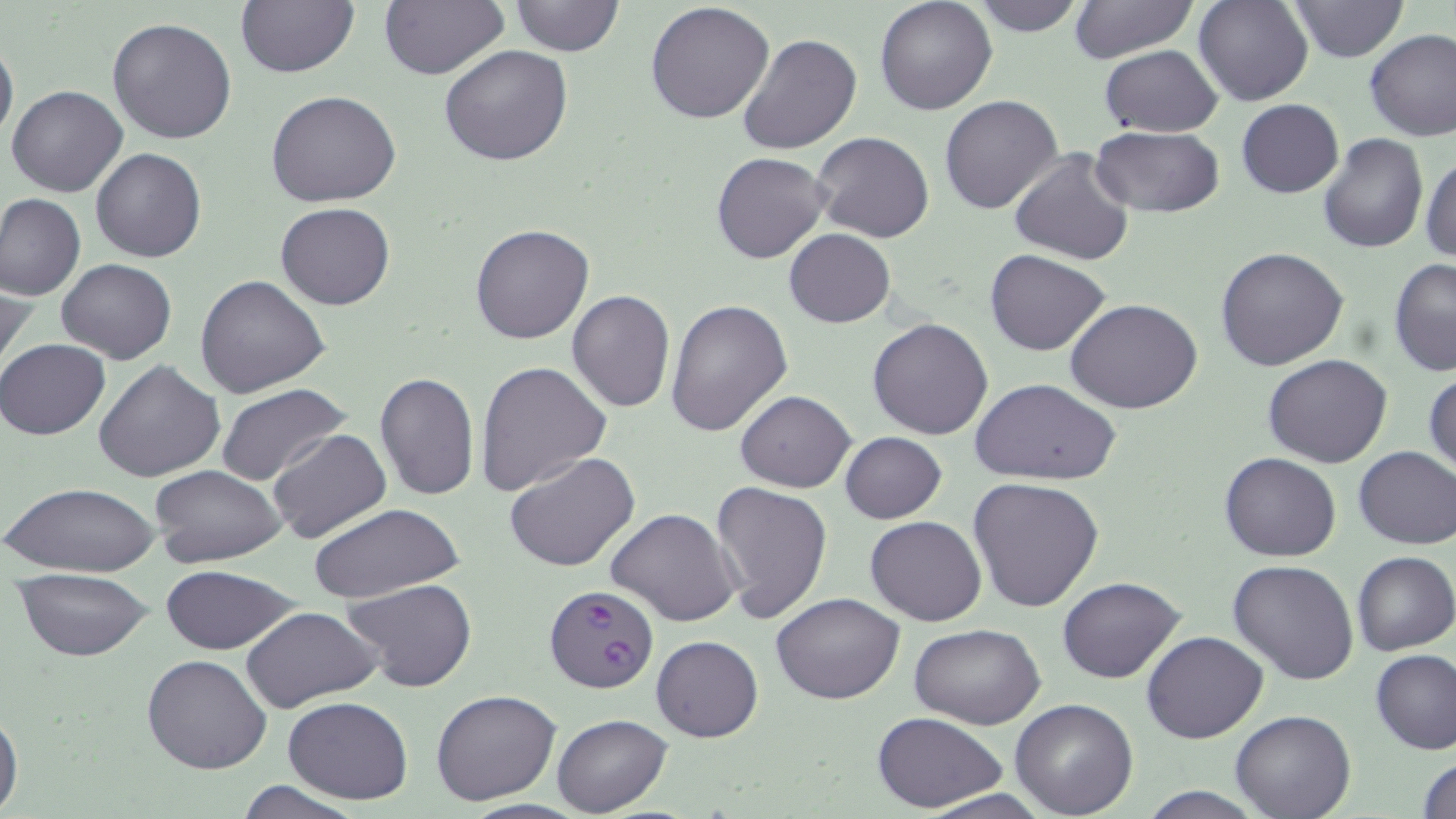

Approximate bounding boxes as [x1, y1, x2, y2] in pixels. Plasmodium falciparum-infected red blood cell locations: [545, 584, 659, 695]. Uninfected red blood cell locations: [234, 0, 359, 78], [377, 0, 509, 80], [508, 0, 625, 56], [874, 0, 998, 116], [968, 0, 1089, 36], [1194, 0, 1312, 106], [1290, 0, 1408, 62], [645, 1, 775, 125], [1065, 1, 1201, 63], [108, 17, 238, 144], [1365, 31, 1456, 143], [736, 32, 861, 155], [0, 35, 18, 147], [440, 44, 573, 166], [1098, 45, 1224, 137], [6, 85, 129, 197], [266, 91, 402, 208], [940, 95, 1063, 214], [1236, 100, 1344, 198], [1089, 126, 1224, 216], [810, 132, 935, 242], [1317, 134, 1428, 255], [91, 147, 206, 263], [1010, 147, 1136, 266], [711, 152, 830, 264], [1421, 152, 1455, 265], [0, 193, 86, 302], [276, 202, 396, 310], [468, 223, 594, 345], [784, 228, 895, 327], [1214, 246, 1351, 371], [986, 250, 1110, 356], [1387, 257, 1455, 377], [56, 258, 177, 364], [1, 268, 36, 378], [194, 275, 331, 398], [567, 288, 676, 412], [665, 298, 793, 437], [1066, 298, 1204, 415], [868, 316, 995, 439], [0, 338, 110, 441], [1263, 354, 1392, 467], [93, 359, 225, 481], [474, 360, 611, 496], [1424, 366, 1456, 481], [374, 370, 480, 501], [972, 378, 1119, 486], [216, 383, 351, 487], [735, 390, 856, 491], [268, 429, 392, 545], [840, 432, 947, 523], [1352, 446, 1456, 549], [504, 451, 641, 573], [1220, 453, 1340, 561], [151, 464, 286, 567], [969, 477, 1105, 613], [5, 481, 160, 578], [710, 481, 833, 625], [306, 504, 463, 603], [607, 508, 742, 627], [864, 514, 987, 625], [1351, 551, 1455, 657], [1229, 558, 1361, 685], [157, 565, 301, 654], [12, 570, 154, 661], [1058, 577, 1185, 684], [343, 578, 476, 693], [771, 591, 904, 705], [242, 606, 382, 712], [909, 624, 1045, 730], [1142, 630, 1268, 743], [651, 634, 764, 742], [1371, 650, 1456, 755], [141, 654, 273, 774], [431, 688, 561, 806], [283, 696, 412, 804], [1010, 698, 1138, 818], [0, 705, 23, 819], [1231, 711, 1356, 819], [870, 712, 1009, 812], [552, 714, 672, 816], [1415, 755, 1456, 819], [234, 780, 363, 818], [916, 788, 1053, 819]. Slide-level diagnosis: Plasmodium falciparum. May-Grünwald-Giemsa-stained preparation. Single field of view. Captured at 1000x magnification. Optical microscopy. Thin blood film. Image is 1456×819 pixels.